Assess this cell for malaria.
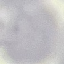

It is uninfected.

image_type: cell patch, automatically extracted from a larger field of view and resized to 64 × 64 pixels
stain: Giemsa
capture: smartphone through the microscope eyepiece
preparation: thin blood film